Comment on the morphology of the red blood cells.
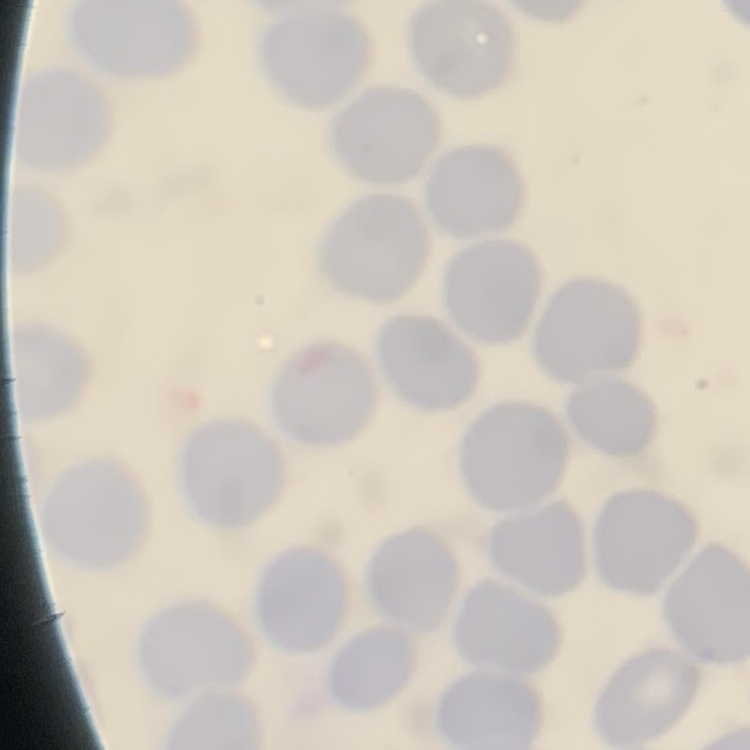
They show no rouleaux formation.

preparation: thin blood smear
stain: Field's or Giemsa
image_type: one tile cut from a larger photomicrograph